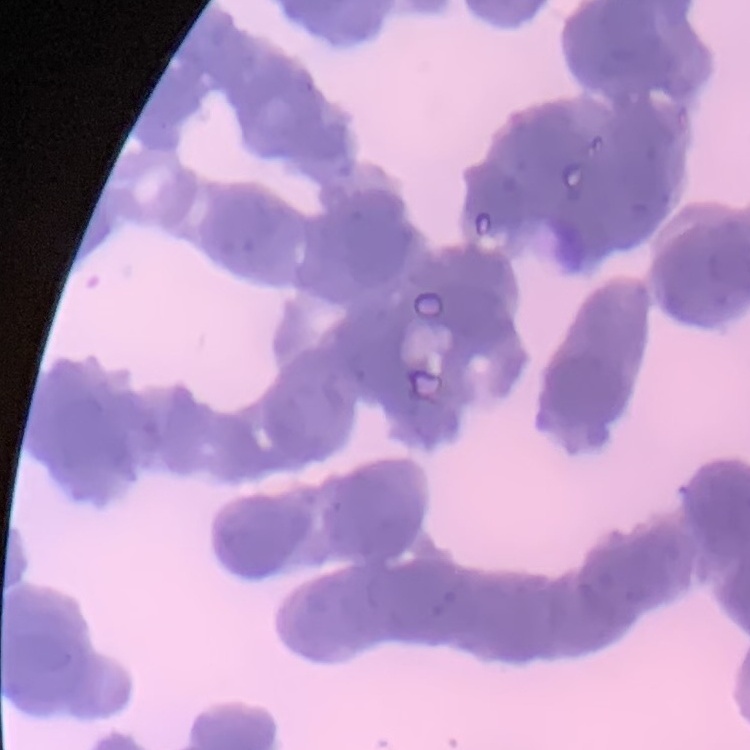 The erythrocytes exhibit rouleaux formation. Thin peripheral smear. Stained with either Field's or Giemsa. One tile cut from a larger photomicrograph.